Report the malaria status of this cell.
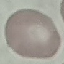
It is uninfected.

Automatically extracted cell patch, resized to 64 × 64 pixels. Thin smear of blood. Giemsa-stained preparation. Photographed with a smartphone camera at the microscope eyepiece.